Locate every Plasmodium falciparum-infected red blood cell.
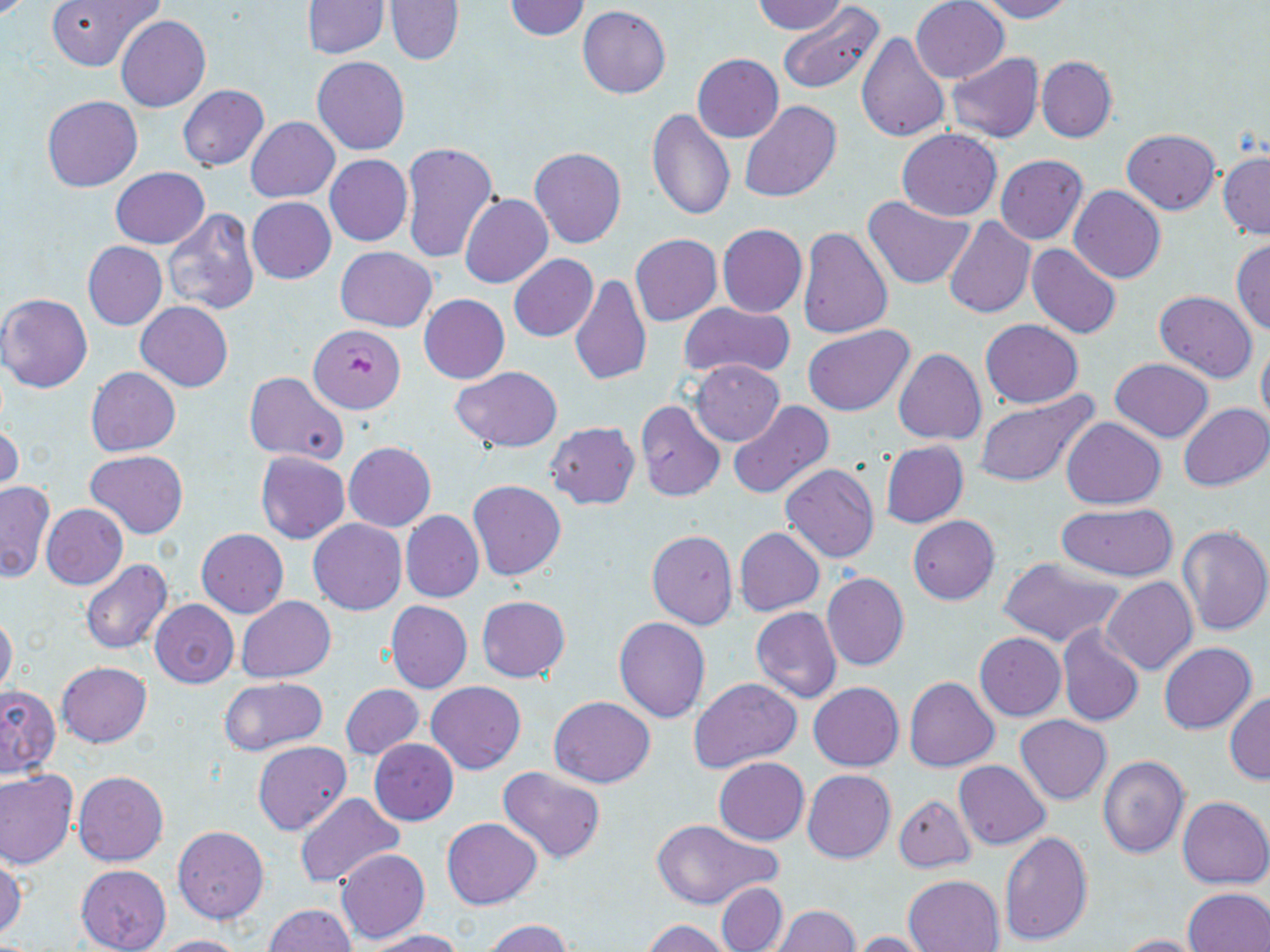

Approximate bounding boxes as (x1, y1, x2, y2) in pixels.
Plasmodium falciparum-infected red blood cells: (310, 325, 405, 413).

Uninfected red blood cell locations: (46, 0, 163, 71), (385, 0, 464, 65), (502, 0, 591, 41), (751, 0, 845, 34), (911, 0, 1008, 83), (973, 0, 1075, 22), (302, 1, 388, 57), (778, 2, 888, 100), (577, 6, 671, 98), (116, 15, 210, 113), (856, 33, 950, 144), (692, 54, 783, 143), (945, 54, 1044, 144), (1036, 55, 1117, 143), (313, 56, 409, 155), (178, 85, 268, 170), (41, 95, 142, 191), (739, 100, 840, 204), (646, 109, 736, 221), (246, 117, 338, 202), (897, 129, 1002, 220), (1122, 129, 1220, 213), (401, 141, 498, 264), (529, 147, 626, 248), (1218, 151, 1270, 239), (326, 155, 412, 246), (995, 155, 1087, 244), (111, 168, 208, 247), (1070, 186, 1165, 283), (459, 194, 552, 288), (863, 196, 974, 290), (248, 197, 336, 284), (164, 208, 260, 314), (943, 217, 1035, 317), (717, 223, 807, 317), (797, 226, 893, 338), (631, 234, 722, 326), (1231, 238, 1270, 337), (83, 241, 167, 330), (1026, 244, 1123, 338), (335, 246, 436, 332), (508, 253, 597, 342), (569, 273, 651, 384), (1154, 291, 1258, 383), (418, 294, 509, 383), (0, 295, 94, 393), (136, 301, 233, 391), (677, 302, 794, 381), (980, 319, 1083, 409), (803, 325, 915, 416), (1257, 338, 1270, 429), (894, 347, 986, 445), (1109, 359, 1215, 441), (690, 360, 785, 446), (85, 367, 180, 455), (450, 367, 560, 452), (243, 371, 349, 465), (974, 391, 1100, 489), (635, 399, 725, 501), (727, 402, 834, 499), (1179, 402, 1270, 491), (1061, 417, 1166, 509), (0, 421, 21, 495), (546, 422, 640, 509), (344, 441, 436, 531), (880, 441, 968, 528), (84, 451, 189, 539), (255, 451, 350, 543), (781, 462, 880, 563), (469, 479, 565, 580), (0, 481, 54, 583), (42, 503, 127, 589), (1055, 504, 1181, 581), (400, 511, 483, 602), (907, 516, 999, 605), (308, 518, 405, 614), (1176, 523, 1270, 637), (734, 527, 824, 615), (197, 528, 288, 618), (646, 529, 739, 629), (998, 556, 1126, 646), (80, 561, 171, 655), (821, 574, 908, 672), (1103, 577, 1197, 675), (477, 595, 569, 682), (236, 596, 336, 682), (150, 600, 238, 688), (385, 601, 472, 693), (751, 606, 841, 703), (0, 613, 17, 696), (614, 617, 711, 723), (1056, 625, 1144, 728), (974, 632, 1066, 721), (1159, 642, 1256, 734), (56, 660, 151, 747), (220, 677, 327, 756), (690, 677, 801, 774), (904, 678, 999, 772), (426, 681, 525, 773), (808, 682, 903, 771), (341, 684, 424, 760), (0, 686, 60, 779), (1225, 690, 1270, 785), (548, 697, 655, 787), (1014, 715, 1112, 805), (369, 739, 459, 825), (253, 741, 352, 835), (1098, 755, 1190, 858), (714, 757, 808, 844), (953, 760, 1051, 851), (498, 767, 604, 863), (802, 769, 895, 863), (0, 770, 77, 869), (73, 771, 168, 866), (295, 792, 404, 890), (893, 795, 976, 873), (1178, 796, 1270, 889), (442, 817, 543, 909), (649, 820, 778, 910), (173, 826, 268, 924), (999, 829, 1092, 945), (337, 849, 430, 943), (0, 855, 25, 939), (76, 865, 171, 952), (902, 874, 1005, 952), (716, 882, 787, 952), (1182, 888, 1270, 952), (265, 904, 356, 952), (772, 905, 860, 951), (641, 919, 735, 952), (481, 920, 574, 951), (364, 929, 466, 952), (852, 930, 936, 951), (1115, 933, 1210, 952), (149, 934, 249, 952). Slide-level diagnosis: Plasmodium falciparum. 1000x magnification. May-Grünwald-Giemsa stain. Optical microscopy. Image is 1270×952 pixels. Thin blood film. Single field of view.